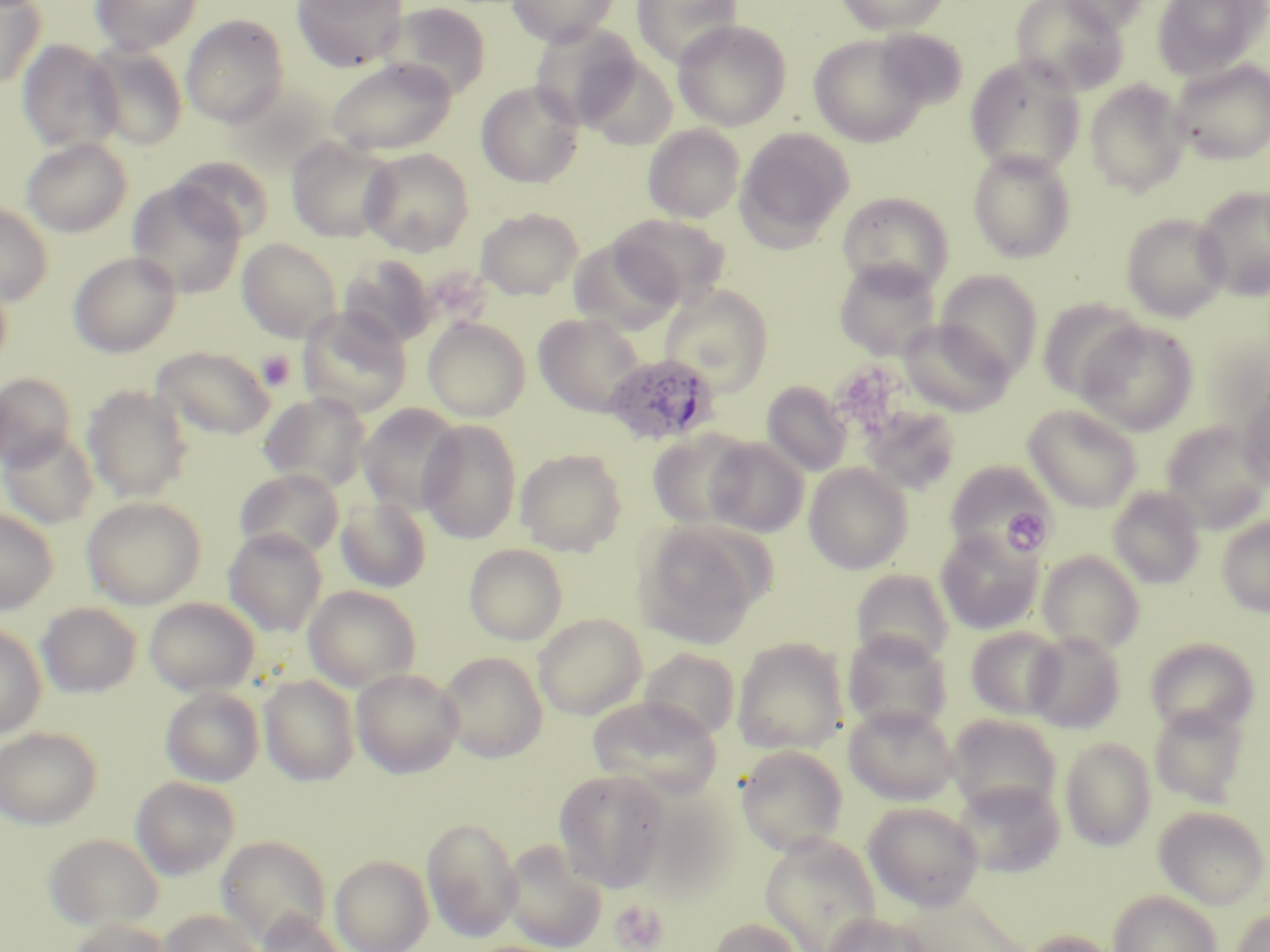

Approximate bounding boxes as (x1, y1, x2, y2) in pixels. Platelet locations: (432, 266, 501, 322), (257, 350, 296, 391), (1001, 506, 1053, 555), (610, 899, 670, 952). Uninfected red blood cell locations: (0, 0, 45, 88), (91, 0, 203, 54), (293, 0, 407, 71), (506, 0, 619, 46), (631, 0, 743, 67), (835, 0, 952, 35), (1011, 0, 1127, 96), (1056, 0, 1154, 33), (1152, 0, 1269, 80), (383, 2, 492, 99), (181, 15, 289, 126), (673, 19, 791, 131), (529, 22, 642, 128), (875, 29, 968, 109), (808, 34, 931, 147), (17, 39, 122, 153), (86, 43, 188, 150), (579, 54, 678, 150), (965, 56, 1085, 177), (326, 57, 457, 156), (1169, 59, 1270, 165), (1083, 79, 1191, 197), (476, 81, 584, 188), (643, 124, 745, 223), (736, 127, 854, 247), (21, 137, 132, 237), (286, 137, 397, 243), (359, 148, 475, 256), (967, 149, 1076, 263), (169, 155, 275, 243), (127, 181, 246, 299), (1193, 186, 1270, 300), (836, 191, 954, 294), (0, 203, 53, 305), (476, 208, 584, 299), (1121, 213, 1230, 322), (612, 214, 731, 308), (237, 238, 341, 341), (569, 238, 681, 336), (68, 251, 182, 357), (340, 256, 437, 348), (833, 259, 941, 360), (937, 270, 1043, 380), (0, 275, 12, 373), (659, 284, 774, 395), (1036, 298, 1145, 401), (297, 306, 413, 418), (533, 313, 648, 418), (423, 317, 531, 421), (898, 319, 1014, 417), (1075, 320, 1198, 435), (151, 345, 276, 440), (0, 372, 78, 470), (762, 381, 852, 477), (82, 384, 193, 503), (1238, 389, 1270, 493), (259, 392, 371, 492), (358, 404, 465, 514), (1023, 404, 1143, 512), (858, 405, 961, 497), (418, 418, 522, 543), (1160, 422, 1269, 532), (1, 428, 98, 528), (647, 430, 756, 530), (704, 437, 809, 537), (515, 448, 627, 556), (945, 461, 1054, 560), (804, 463, 912, 574), (234, 468, 345, 560), (1107, 486, 1206, 588), (334, 495, 432, 593), (82, 496, 207, 609), (0, 508, 58, 614), (1216, 514, 1270, 617), (636, 521, 767, 649), (223, 529, 327, 636), (935, 529, 1042, 634), (935, 542, 1144, 642), (464, 543, 568, 645), (1036, 550, 1145, 656), (851, 569, 954, 668), (304, 585, 421, 691), (144, 597, 260, 696), (36, 602, 142, 698), (533, 613, 645, 719), (0, 624, 47, 741), (965, 626, 1067, 720), (843, 631, 952, 735), (1025, 631, 1126, 733), (1144, 637, 1259, 737), (732, 638, 848, 754), (638, 647, 740, 740), (439, 651, 548, 762), (351, 668, 463, 779), (259, 674, 360, 786), (160, 686, 264, 786), (588, 696, 722, 797), (844, 704, 960, 805), (1149, 704, 1249, 807), (947, 714, 1062, 818), (0, 727, 102, 829), (1059, 737, 1156, 851), (736, 744, 848, 856), (553, 769, 672, 892), (131, 775, 241, 879), (952, 779, 1066, 877), (636, 791, 737, 902), (863, 801, 984, 911), (1154, 806, 1269, 909), (422, 816, 521, 941), (44, 833, 164, 932), (760, 833, 883, 952), (217, 835, 331, 944), (501, 839, 607, 952), (330, 855, 434, 952), (1109, 890, 1221, 952), (898, 892, 1031, 952), (160, 909, 263, 952), (1230, 909, 1270, 952), (254, 911, 347, 952), (821, 911, 932, 952), (68, 917, 170, 952), (707, 917, 807, 952), (1019, 930, 1124, 952). Plasmodium ovale-infected red blood cell locations: (604, 352, 721, 446). Slide-level diagnosis: Plasmodium ovale. 1000x magnification. Optical microscopy. Thin blood smear. Image is 1270×952 pixels. One field of a larger specimen. May-Grünwald-Giemsa stain.